Classify this cell by malaria status.
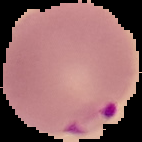
It is parasitized.

Image is 142×142 pixels. The area outside the segmented cell region is set to black. From a thin blood film.